Assess this cell for malaria.
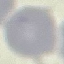
It is uninfected.

preparation = thin blood smear
capture = smartphone through the microscope eyepiece
image type = automatically extracted cell patch, resized to 64 × 64 pixels
stain = Giemsa